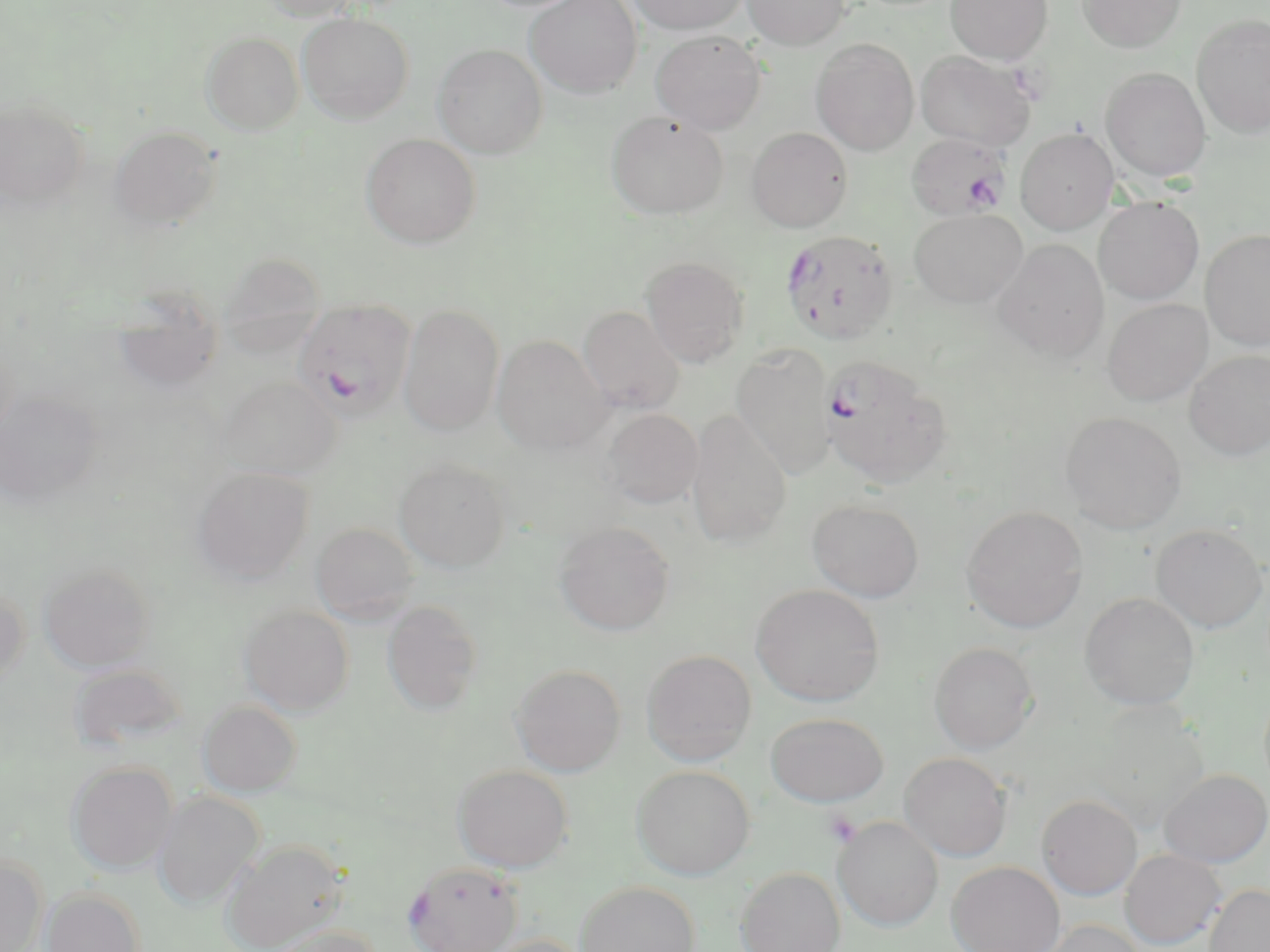

Approximate bounding boxes as (x1, y1, x2, y2) in pixels. Uninfected red blood cell locations: (259, 0, 364, 21), (525, 0, 643, 98), (626, 0, 747, 35), (742, 0, 850, 49), (946, 0, 1053, 64), (1077, 0, 1186, 52), (298, 12, 414, 124), (1192, 15, 1270, 138), (651, 30, 766, 134), (202, 32, 303, 135), (812, 39, 919, 155), (433, 44, 548, 158), (915, 51, 1037, 151), (1101, 67, 1211, 182), (0, 98, 89, 211), (606, 111, 728, 220), (109, 125, 222, 233), (747, 127, 852, 232), (1015, 128, 1118, 234), (361, 134, 481, 249), (1094, 197, 1203, 304), (909, 209, 1027, 308), (1201, 228, 1270, 351), (994, 239, 1109, 362), (220, 253, 326, 355), (640, 255, 749, 368), (111, 290, 226, 394), (1102, 298, 1212, 406), (398, 304, 504, 436), (577, 306, 685, 415), (492, 334, 612, 455), (731, 343, 837, 477), (1185, 350, 1270, 461), (218, 376, 341, 479), (0, 389, 105, 510), (601, 408, 703, 509), (686, 410, 793, 548), (1060, 411, 1187, 534), (394, 458, 511, 572), (192, 466, 314, 583), (808, 499, 924, 602), (961, 506, 1087, 632), (311, 522, 418, 624), (555, 522, 674, 636), (1150, 523, 1268, 633), (39, 562, 156, 672), (0, 582, 29, 689), (751, 584, 885, 707), (1080, 591, 1200, 710), (381, 600, 483, 715), (238, 604, 355, 715), (929, 642, 1038, 753), (641, 649, 757, 765), (68, 662, 188, 752), (511, 663, 627, 776), (198, 700, 302, 797), (1089, 705, 1210, 829), (765, 712, 889, 807), (899, 752, 1013, 861), (65, 760, 178, 874), (453, 764, 573, 872), (632, 764, 754, 880), (1159, 769, 1269, 867), (153, 791, 264, 910), (1036, 794, 1143, 900), (832, 816, 943, 932), (219, 838, 349, 951), (1119, 849, 1226, 950), (0, 854, 48, 952), (947, 861, 1065, 952), (736, 866, 845, 952), (575, 881, 701, 952), (1203, 883, 1270, 952), (40, 887, 145, 952), (1037, 919, 1148, 952), (266, 924, 383, 952), (482, 934, 591, 952). Platelet locations: (823, 808, 861, 847). Plasmodium falciparum-infected red blood cell locations: (906, 133, 1014, 220), (779, 229, 899, 345), (293, 298, 416, 421), (819, 355, 952, 488), (403, 861, 522, 952). Slide-level diagnosis: Plasmodium falciparum. Single field of view. Image is 1270×952 pixels. Thin blood film. Captured at 1000x magnification. Light microscopy. May-Grünwald-Giemsa-stained preparation.